Give the position of every malaria parasite.
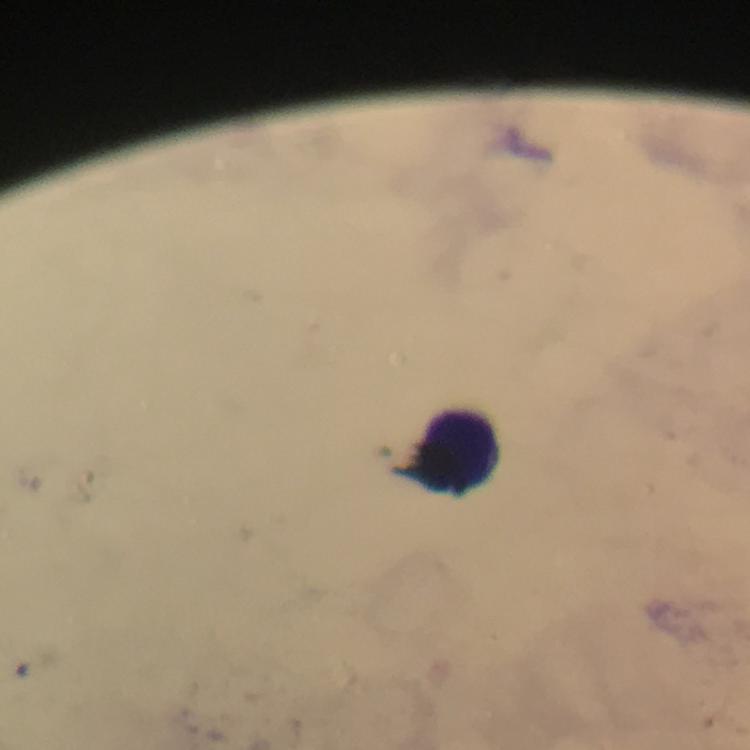
No malaria parasites seen.

Approximate centers as [x, y] in pixels. Leukocyte locations: [456, 451]. A crop from one field of view. Image is 750×750 pixels. 100x magnification. Immersion oil was used. Thick blood smear. Photographed through the microscope with a smartphone camera. Giemsa stain. From a diagnostic examination for malaria.